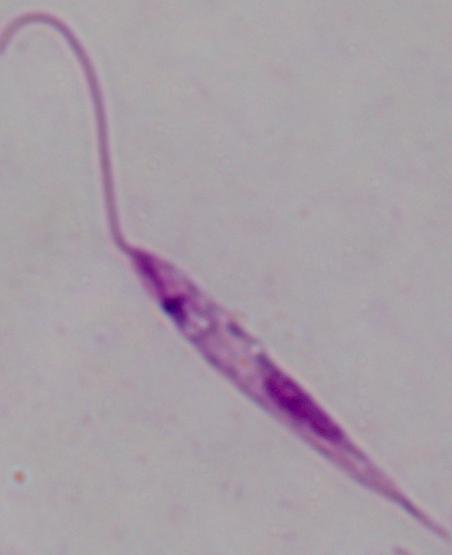
A Leishmania parasite is shown. 1000x magnification. Photomicrograph.